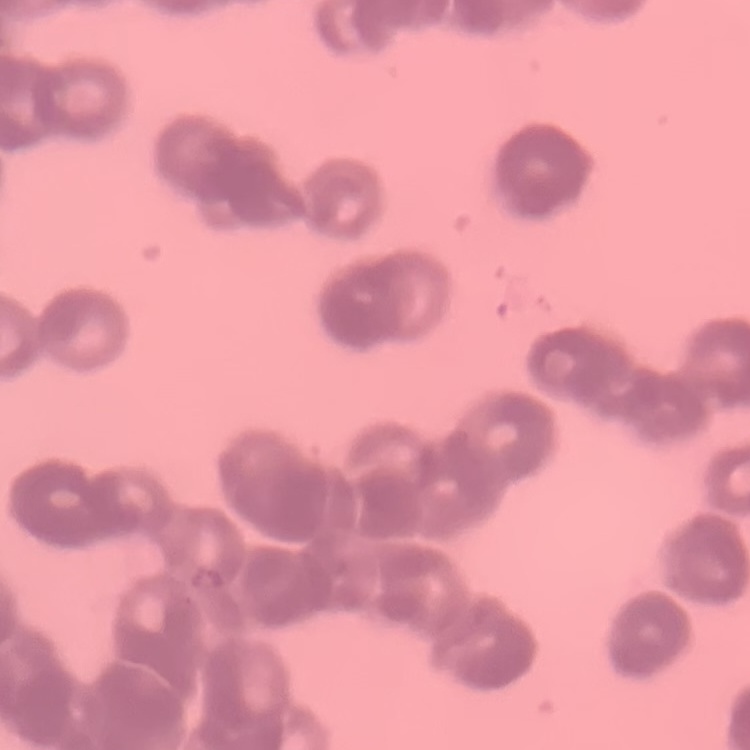
erythrocyte morphology = rouleaux formation
preparation = thin blood smear
stain = Field's or Giemsa
image type = square crop of a larger photomicrograph